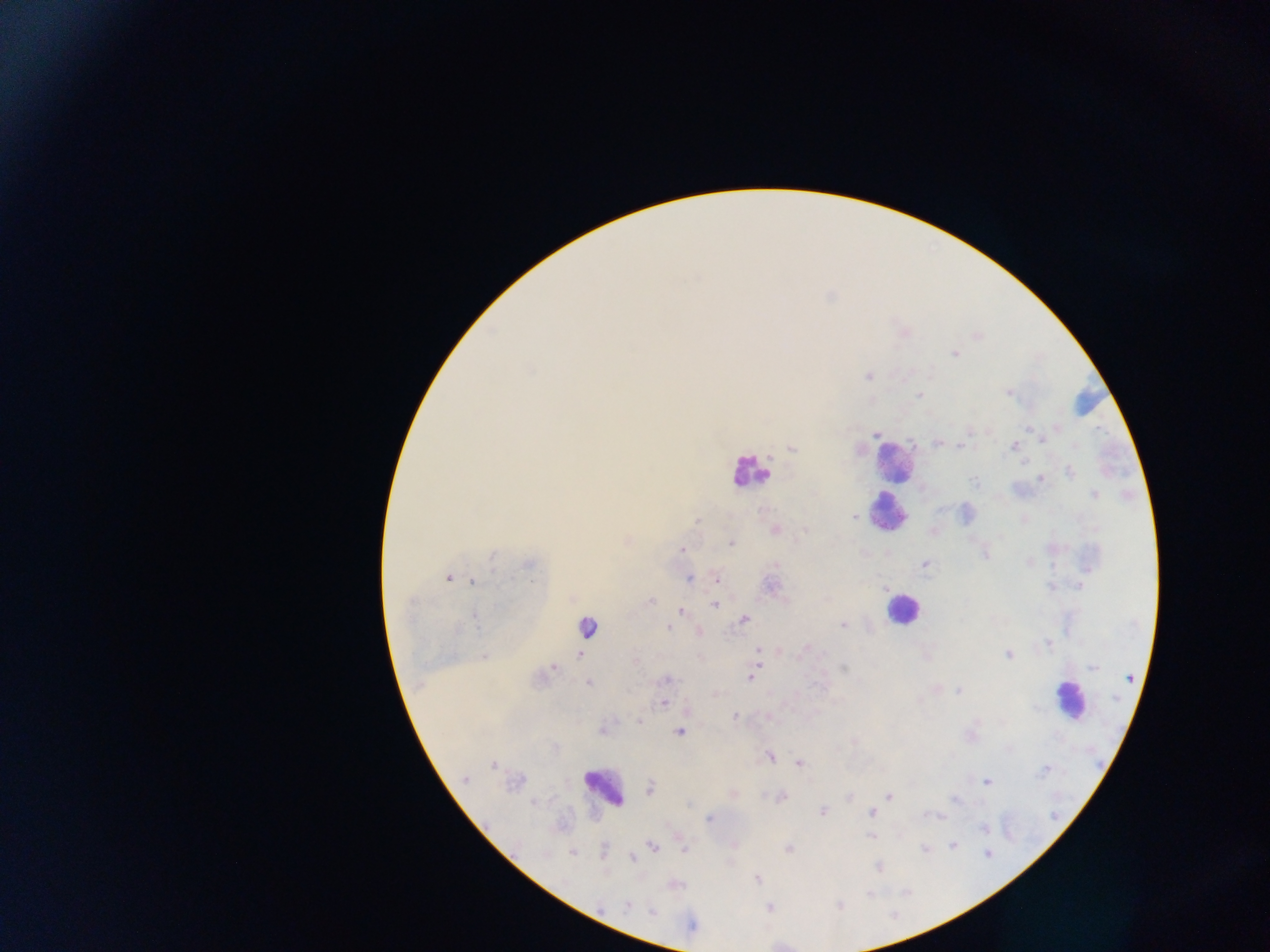 Approximate centers as [x, y] in pixels. Leukocyte locations: [1089, 401], [893, 462], [749, 470], [887, 513], [901, 609], [586, 627], [1070, 700], [603, 788]. Plasmodium parasite locations: [976, 337], [954, 353], [867, 376], [1008, 392], [920, 394], [1027, 427], [875, 432], [1042, 439], [938, 442], [962, 446], [1013, 446], [791, 447], [1069, 472], [1042, 479], [1094, 496], [853, 517], [696, 520], [774, 529], [933, 531], [731, 543], [682, 549], [985, 553], [1027, 562], [924, 565], [448, 578], [689, 578], [716, 580], [474, 581], [650, 600], [714, 604], [681, 612], [744, 619], [843, 624], [668, 628], [697, 631], [1049, 644], [806, 647], [758, 649], [580, 654], [1009, 655], [484, 656], [757, 660], [635, 663], [553, 666], [1093, 666], [845, 667], [753, 673], [750, 677], [666, 679], [589, 682], [936, 688], [958, 691], [663, 702], [686, 711], [734, 717], [766, 717], [638, 722], [602, 732], [680, 732], [852, 741], [770, 757], [798, 763], [493, 765], [464, 780], [987, 782], [650, 788], [733, 793], [849, 796], [888, 796], [780, 797], [822, 812], [870, 812], [710, 818], [871, 836], [679, 838], [733, 844], [953, 845], [652, 847], [684, 849], [788, 849], [924, 849], [572, 852], [987, 852], [631, 858], [877, 867], [757, 878], [628, 906], [769, 908]. Collected in Ghana. Image is 1270×952 pixels. One field of view. Mobile-phone photograph taken through the microscope. Thick blood smear.